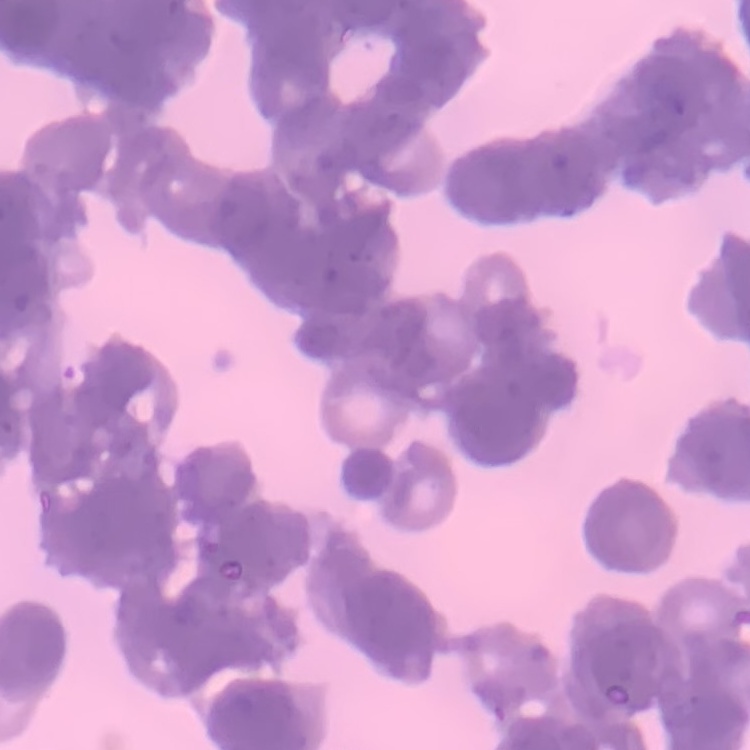

Summary:
  - Erythrocyte morphology: rouleaux formation
  - Stain: Field's or Giemsa
  - Preparation: thin blood film
  - Image type: one tile cut from a larger photomicrograph